State which cell type is depicted.
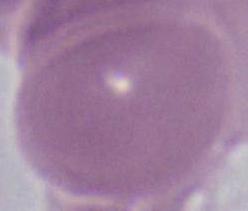

An erythrocyte.

Summary:
  - Modality: micrograph
  - Magnification: 1000x